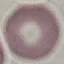

malaria_status: uninfected
capture: smartphone through the microscope eyepiece
image_type: cell patch, automatically extracted from a larger field of view and resized to 64 × 64 pixels
preparation: thin blood film
stain: Giemsa